Report the malaria status of this cell.
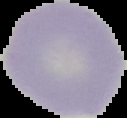
It is uninfected.

{
  "image_size": "127×118 pixels",
  "preparation": "thin blood film",
  "image_type": "segmented cell region on a black background"
}